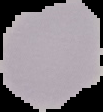
Summary:
  - Result: no malaria parasites seen
  - Preparation: thin blood smear
  - Image type: segmented cell region with the area outside set to black
  - Image size: 103×112 pixels